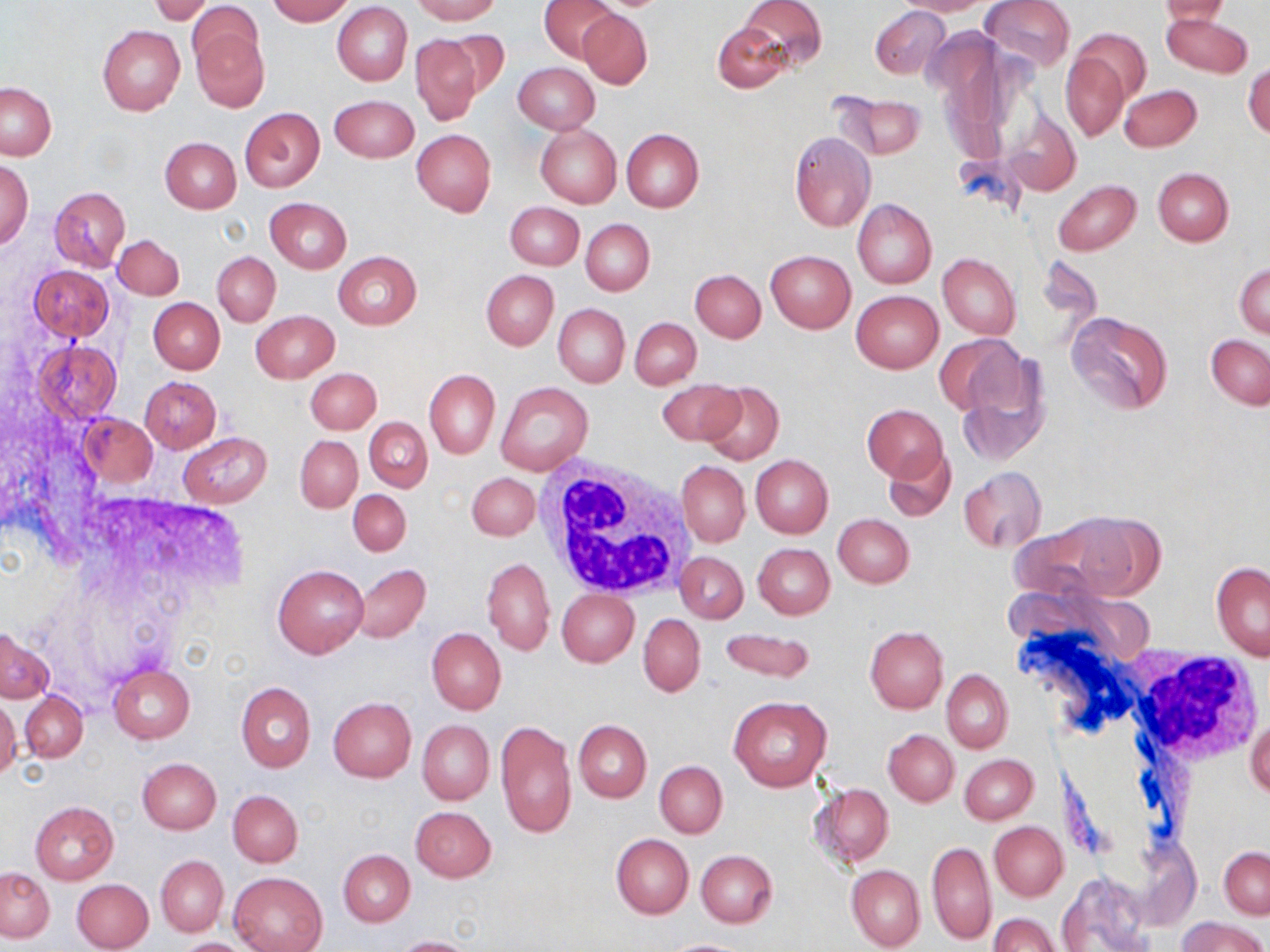

{
  "slide_level_diagnosis": "negative for blood parasites",
  "preparation": "thin blood film",
  "magnification": "1000x",
  "uninfected_red_blood_cell_locations": "approximate bounding boxes as [x1, y1, x2, y2] in pixels: [267, 0, 353, 24], [411, 0, 499, 24], [538, 0, 616, 63], [741, 0, 826, 72], [894, 0, 995, 15], [981, 0, 1075, 71], [151, 1, 212, 25], [1160, 1, 1231, 24], [332, 2, 413, 85], [189, 3, 262, 72], [870, 6, 949, 80], [578, 10, 652, 89], [1162, 13, 1252, 77], [190, 20, 268, 111], [713, 21, 790, 93], [97, 24, 186, 116], [1064, 30, 1148, 140], [444, 31, 511, 100], [412, 36, 482, 125], [1244, 61, 1270, 139], [513, 62, 599, 134], [1, 83, 56, 160], [1119, 85, 1201, 153], [833, 92, 927, 160], [329, 94, 419, 163], [240, 107, 324, 191], [1005, 110, 1081, 196], [534, 124, 621, 208], [411, 129, 496, 216], [621, 129, 704, 213], [788, 131, 875, 231], [160, 138, 241, 213], [0, 160, 32, 247], [1153, 168, 1234, 246], [1055, 180, 1141, 255], [50, 187, 130, 271], [265, 197, 351, 274], [852, 199, 936, 288], [505, 201, 583, 270], [581, 219, 654, 296], [114, 234, 184, 300], [765, 250, 856, 332], [334, 251, 422, 329], [213, 252, 280, 327], [937, 253, 1020, 338], [1234, 262, 1270, 337], [28, 265, 113, 340], [481, 270, 557, 349], [690, 270, 765, 342], [851, 291, 943, 373], [148, 299, 224, 374], [553, 303, 630, 387], [251, 310, 338, 382], [1067, 311, 1172, 414], [631, 318, 701, 389], [934, 333, 1027, 422], [1206, 334, 1270, 408], [31, 340, 123, 422], [952, 346, 1051, 464], [306, 368, 381, 434], [424, 370, 500, 458], [139, 376, 220, 453], [657, 378, 743, 447], [495, 382, 593, 476], [699, 382, 786, 466], [863, 404, 947, 482], [76, 412, 157, 487], [363, 417, 432, 492], [179, 432, 271, 509], [295, 435, 362, 512], [882, 447, 957, 522], [750, 455, 833, 538], [676, 460, 749, 546], [959, 468, 1045, 551], [468, 473, 540, 540], [348, 489, 411, 556], [1060, 512, 1164, 599], [833, 514, 915, 588], [753, 544, 835, 619], [676, 551, 748, 624], [481, 556, 555, 656], [1210, 561, 1270, 660], [274, 564, 368, 659], [352, 564, 430, 642], [557, 589, 639, 667], [638, 614, 705, 697], [865, 626, 948, 713], [426, 627, 506, 716], [717, 628, 817, 684], [0, 630, 52, 702], [109, 663, 195, 743], [942, 669, 1013, 752], [235, 681, 316, 772], [20, 691, 88, 762], [728, 694, 833, 791], [328, 696, 417, 782], [0, 697, 21, 783], [1247, 713, 1270, 803], [417, 719, 494, 805], [495, 719, 577, 840], [573, 720, 651, 802], [884, 729, 959, 806], [960, 754, 1037, 824], [137, 758, 220, 835], [655, 760, 727, 838], [809, 784, 894, 869], [228, 790, 302, 867], [29, 802, 118, 884], [410, 806, 497, 882], [989, 821, 1066, 901], [612, 834, 693, 919], [926, 841, 996, 946], [1219, 847, 1270, 919], [338, 848, 415, 926], [696, 849, 777, 928], [156, 855, 229, 937], [845, 865, 925, 951], [0, 867, 54, 942], [229, 871, 327, 952], [1058, 872, 1154, 952], [73, 879, 154, 952], [988, 913, 1060, 952], [1178, 916, 1265, 952], [393, 936, 479, 952], [173, 937, 258, 951], [663, 938, 752, 952]",
  "modality": "optical microscopy",
  "image_size": "1270×952 pixels",
  "white_blood_cell_locations": "approximate bounding boxes as [x1, y1, x2, y2] in pixels: [534, 456, 700, 601], [1130, 648, 1266, 765]",
  "stain": "May-Grünwald-Giemsa",
  "field_of_view": "one of a larger specimen"
}